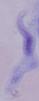
Summary:
  - Modality: photomicrograph
  - Magnification: 1000x
  - Identification: trypanosome